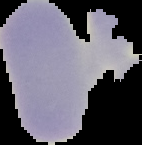

Segmented cell region on a black background. From a thin blood film. Image is 142×145 pixels. Malaria status: uninfected.